State which parasite is depicted.
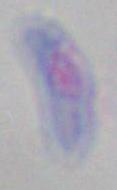
Toxoplasma gondii.

Summary:
  - Magnification: 1000x
  - Modality: photomicrograph